Classify this cell by malaria status.
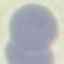

It is uninfected.

Giemsa stain. Photographed with a smartphone camera at the microscope eyepiece. Thin smear of blood. Cell patch, automatically extracted from a larger field of view and resized to 64 × 64 pixels.